Identify the blood parasite species.
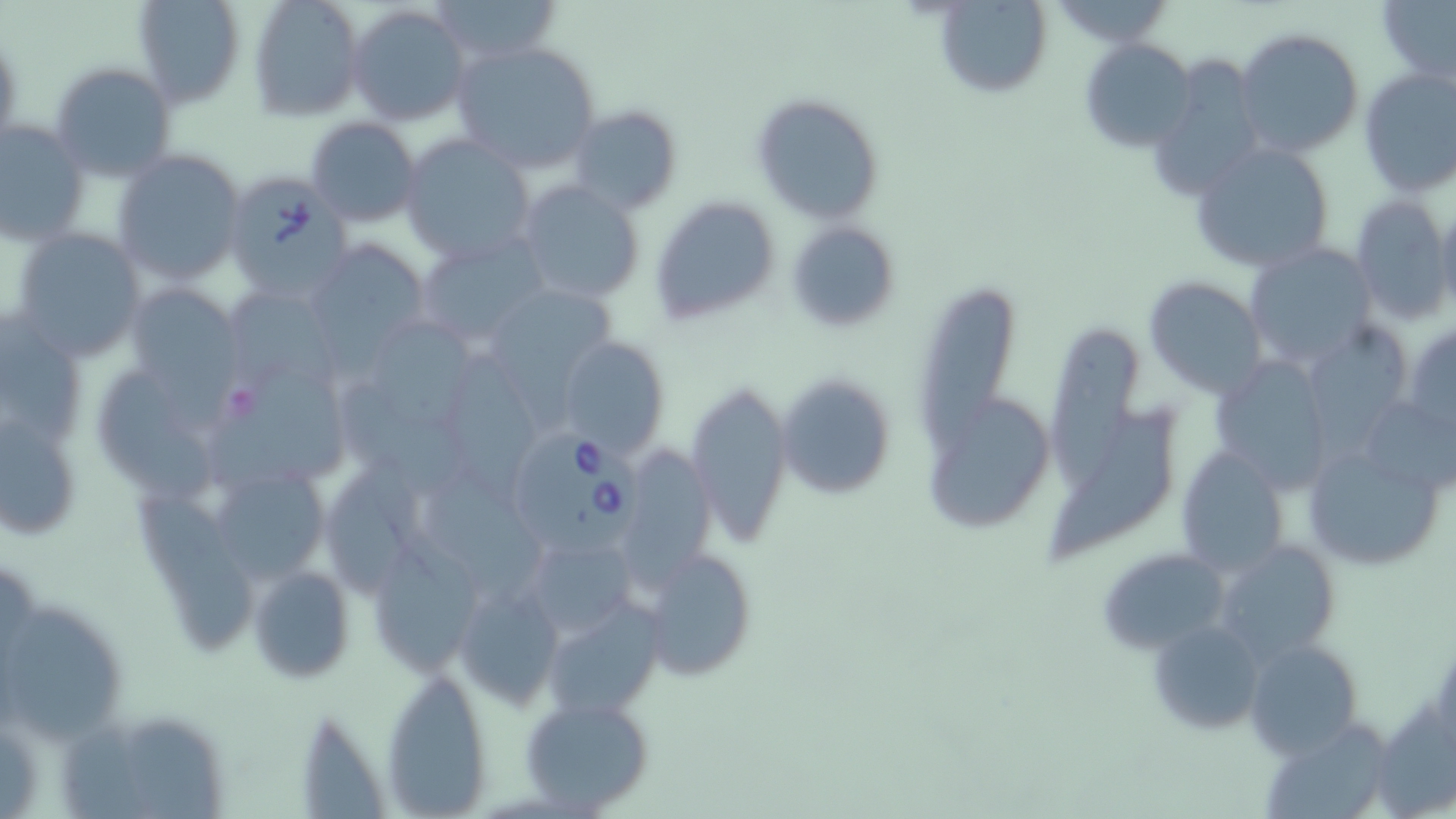
Babesia divergens.

{
  "image_size": "1456×819 pixels",
  "babesia_divergens_infected_red_blood_cell_locations": "approximate bounding boxes as [x1, y1, x2, y2] in pixels: [223, 169, 352, 301], [516, 426, 645, 554]",
  "magnification": "1000x",
  "stain": "May-Grünwald-Giemsa",
  "preparation": "thin blood smear",
  "uninfected_red_blood_cell_locations": "approximate bounding boxes as [x1, y1, x2, y2] in pixels: [132, 0, 245, 107], [248, 0, 364, 122], [425, 0, 560, 65], [1378, 0, 1456, 85], [935, 1, 1051, 100], [347, 4, 472, 127], [1236, 28, 1364, 160], [1079, 36, 1197, 151], [450, 41, 602, 174], [1150, 57, 1266, 202], [49, 61, 177, 182], [1357, 66, 1456, 197], [752, 92, 883, 223], [569, 105, 682, 214], [304, 116, 423, 227], [0, 117, 90, 246], [400, 136, 536, 265], [1187, 141, 1335, 273], [110, 149, 246, 286], [515, 180, 645, 306], [1350, 194, 1453, 324], [650, 196, 780, 326], [1436, 201, 1456, 316], [786, 221, 900, 334], [8, 227, 147, 363], [416, 235, 553, 346], [307, 240, 431, 356], [1245, 243, 1376, 368], [225, 275, 344, 389], [1145, 275, 1267, 398], [916, 282, 1015, 459], [125, 283, 246, 407], [493, 287, 610, 419], [0, 308, 87, 452], [1305, 319, 1412, 461], [1406, 321, 1456, 440], [379, 322, 479, 435], [1054, 331, 1139, 495], [553, 337, 669, 456], [1208, 346, 1327, 492], [452, 351, 540, 504], [215, 353, 355, 491], [776, 372, 896, 500], [343, 374, 474, 503], [101, 377, 224, 502], [686, 382, 790, 547], [1046, 397, 1177, 567], [927, 398, 1053, 533], [1, 403, 84, 542], [1362, 403, 1456, 488], [1305, 432, 1449, 573], [627, 445, 715, 589], [1175, 447, 1287, 576], [323, 457, 428, 595], [206, 460, 335, 588], [424, 469, 546, 602], [135, 493, 262, 654], [521, 531, 632, 642], [366, 538, 485, 675], [1218, 538, 1341, 665], [638, 546, 758, 682], [1098, 546, 1229, 652], [250, 563, 357, 684], [451, 580, 565, 710], [2, 599, 130, 740], [544, 603, 665, 720], [1145, 616, 1264, 736], [1245, 638, 1363, 758], [379, 667, 494, 816], [518, 694, 657, 816], [1375, 695, 1456, 819], [77, 707, 234, 819], [1266, 721, 1384, 819]",
  "modality": "light microscopy",
  "field_of_view": "single"
}